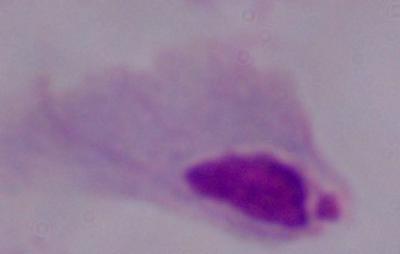 Captured at 1000x magnification. A trichomonad is shown. Micrograph.